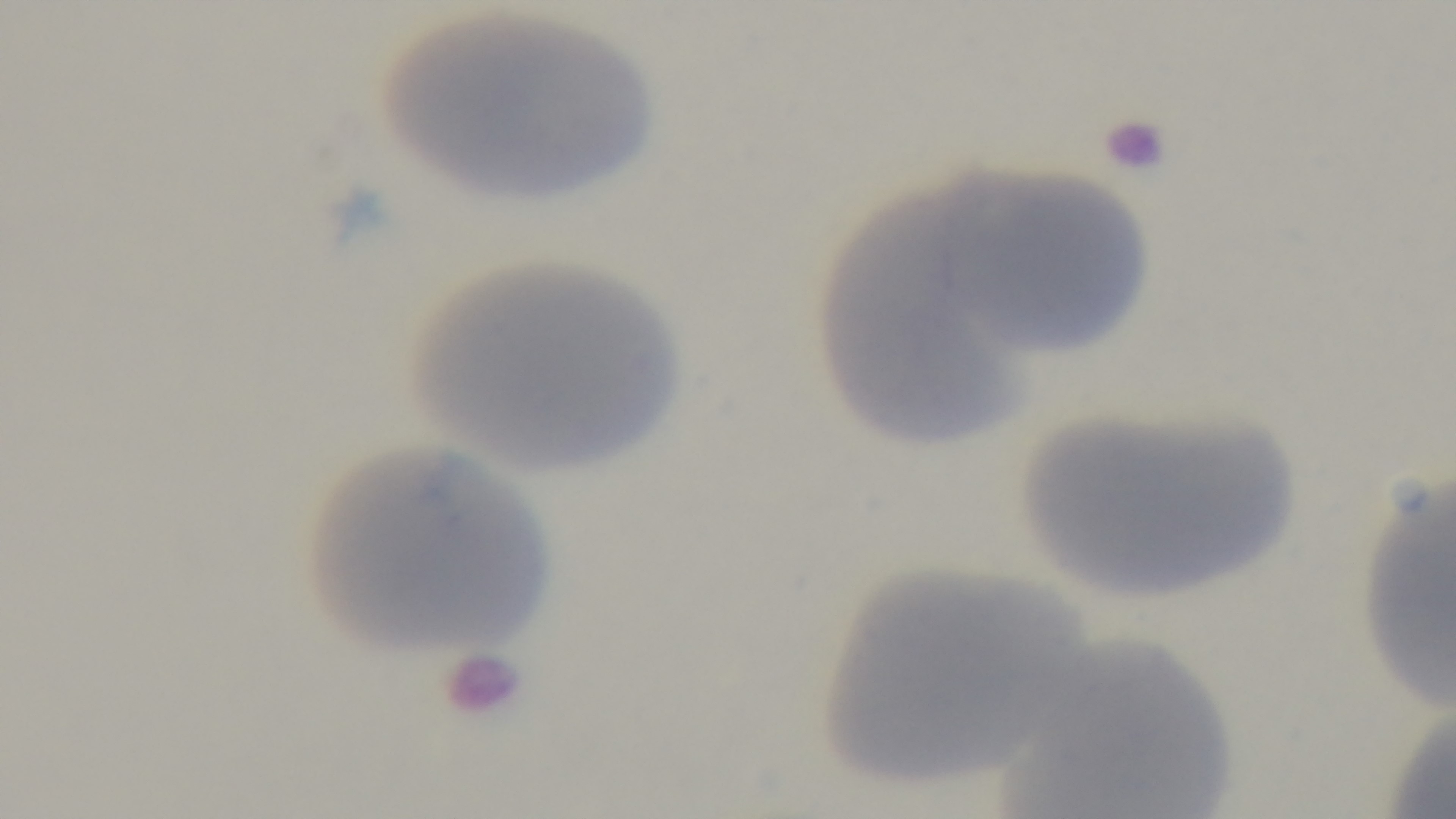
One field from the slide. Mounted 4K digital camera. Preparation: thin. 100x oil-immersion objective. Photomicrograph. Giemsa-stained. Malaria status: negative.